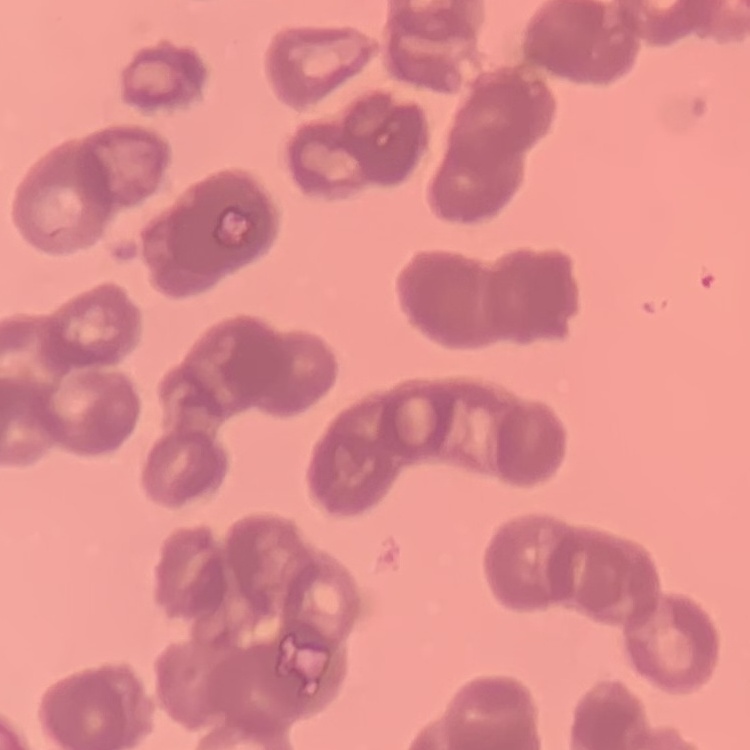

erythrocyte morphology = rouleaux formation
image type = square crop of a larger photomicrograph
preparation = thin blood film
stain = Field's or Giemsa